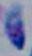
Summary:
  - Magnification: 1000x
  - Identification: Toxoplasma gondii
  - Modality: micrograph